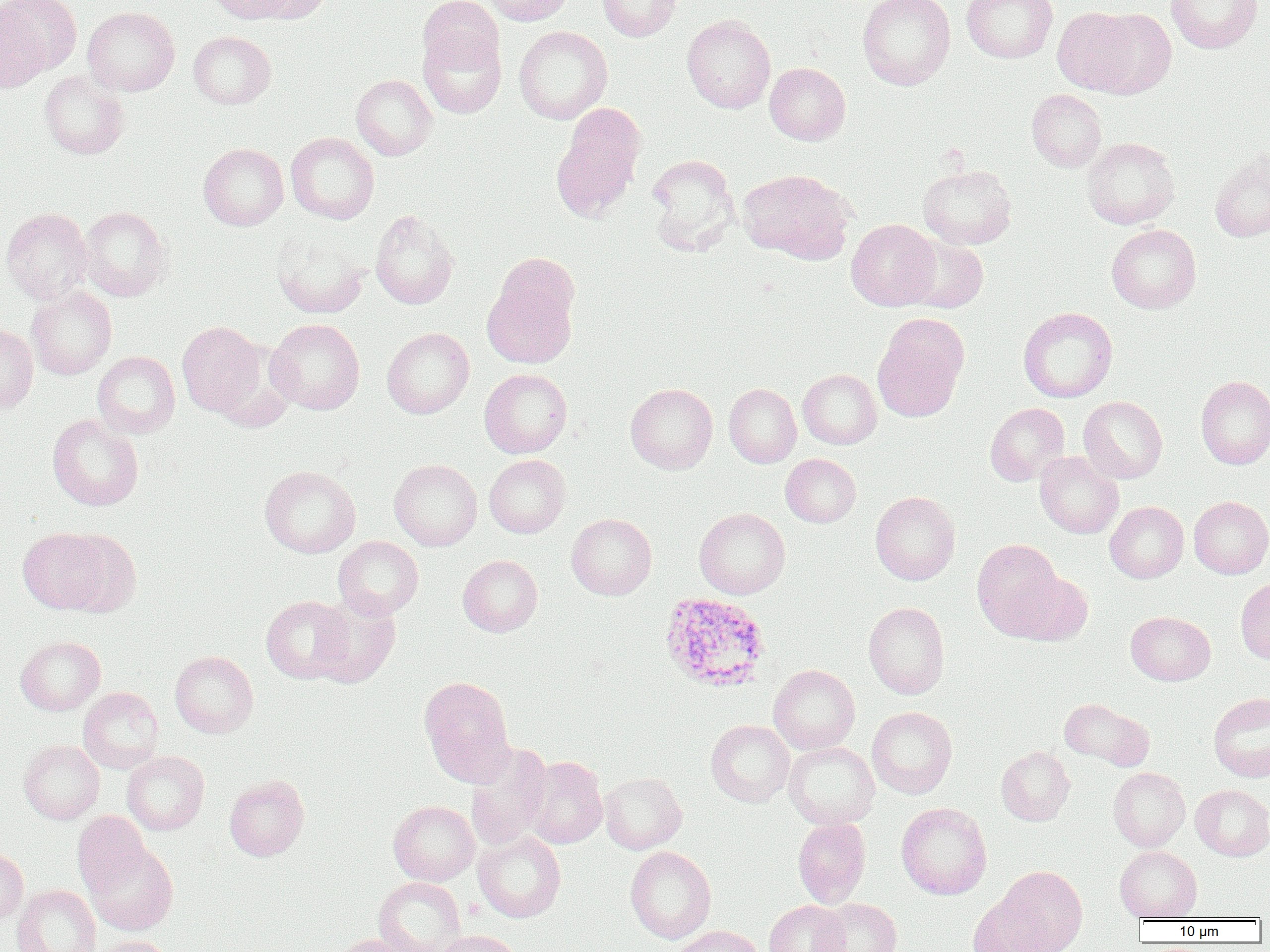
plasmodium_ovale_infected_red_blood_cell_locations: 'approximate bounding boxes as [x1, y1, x2, y2] in pixels: [659, 592, 770, 692]'
slide_level_diagnosis: Plasmodium ovale
image_size: 1270×952 pixels
magnification: 1000x
modality: optical microscopy
preparation: thin blood film
uninfected_red_blood_cell_locations: 'approximate bounding boxes as [x1, y1, x2, y2] in pixels: [1, 0, 82, 74], [208, 0, 295, 24], [247, 0, 331, 24], [418, 0, 503, 70], [482, 0, 574, 25], [597, 0, 681, 41], [857, 0, 955, 90], [961, 0, 1057, 63], [1166, 1, 1263, 53], [82, 6, 180, 97], [1051, 7, 1141, 95], [1089, 9, 1177, 98], [682, 14, 776, 113], [514, 26, 613, 124], [418, 29, 506, 118], [188, 31, 276, 108], [764, 62, 850, 145], [39, 70, 129, 159], [351, 74, 437, 160], [1027, 89, 1107, 171], [551, 106, 645, 221], [285, 132, 379, 224], [1082, 137, 1180, 229], [198, 143, 288, 230], [1210, 150, 1270, 242], [646, 154, 739, 253], [918, 165, 1017, 249], [737, 169, 855, 263], [79, 205, 170, 301], [1, 207, 92, 303], [370, 210, 458, 309], [846, 219, 940, 310], [1106, 224, 1201, 313], [272, 227, 370, 319], [902, 235, 988, 313], [482, 273, 578, 369], [26, 286, 117, 380], [1018, 307, 1118, 402], [872, 315, 969, 422], [266, 318, 365, 415], [177, 321, 268, 418], [0, 322, 39, 414], [382, 327, 474, 419], [92, 351, 180, 438], [479, 369, 572, 458], [798, 369, 881, 449], [1196, 375, 1270, 469], [625, 383, 718, 473], [724, 383, 802, 468], [1078, 396, 1167, 483], [985, 403, 1070, 486], [47, 414, 144, 511], [1035, 451, 1124, 538], [781, 454, 861, 527], [484, 455, 570, 538], [389, 459, 482, 550], [259, 465, 360, 557], [870, 491, 960, 585], [1189, 496, 1270, 578], [1105, 501, 1188, 583], [694, 508, 790, 599], [567, 513, 657, 599], [18, 527, 113, 615], [55, 531, 142, 617], [333, 536, 424, 619], [972, 539, 1066, 638], [457, 555, 542, 637], [1009, 569, 1093, 646], [1236, 577, 1270, 664], [261, 595, 354, 683], [310, 595, 400, 687], [863, 602, 950, 699], [1126, 611, 1215, 685], [15, 636, 105, 715], [170, 650, 258, 738], [768, 665, 860, 754], [418, 676, 516, 784], [78, 687, 163, 773], [1208, 691, 1270, 782], [1059, 698, 1154, 771], [867, 707, 957, 799], [705, 719, 794, 807], [19, 740, 104, 824], [784, 741, 880, 829], [466, 743, 551, 849], [996, 745, 1075, 826], [122, 751, 209, 835], [523, 756, 608, 848], [1108, 767, 1190, 851], [599, 772, 687, 854], [224, 775, 309, 860], [1191, 784, 1270, 860], [388, 801, 479, 885], [896, 802, 992, 900], [72, 811, 150, 896], [793, 816, 871, 908], [473, 831, 566, 922], [85, 840, 178, 936], [1115, 845, 1202, 921], [0, 846, 28, 926], [625, 846, 717, 944], [996, 865, 1087, 952], [374, 876, 466, 952], [12, 884, 101, 952], [967, 894, 1057, 952], [815, 898, 901, 952], [764, 899, 849, 952], [669, 925, 764, 952], [433, 930, 522, 952], [335, 934, 417, 952], [94, 935, 177, 952]'
field_of_view: one of a larger specimen